Name the cell type shown.
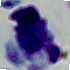

This is a leukocyte.

modality = photomicrograph
magnification = 1000x